Name the blood parasite species.
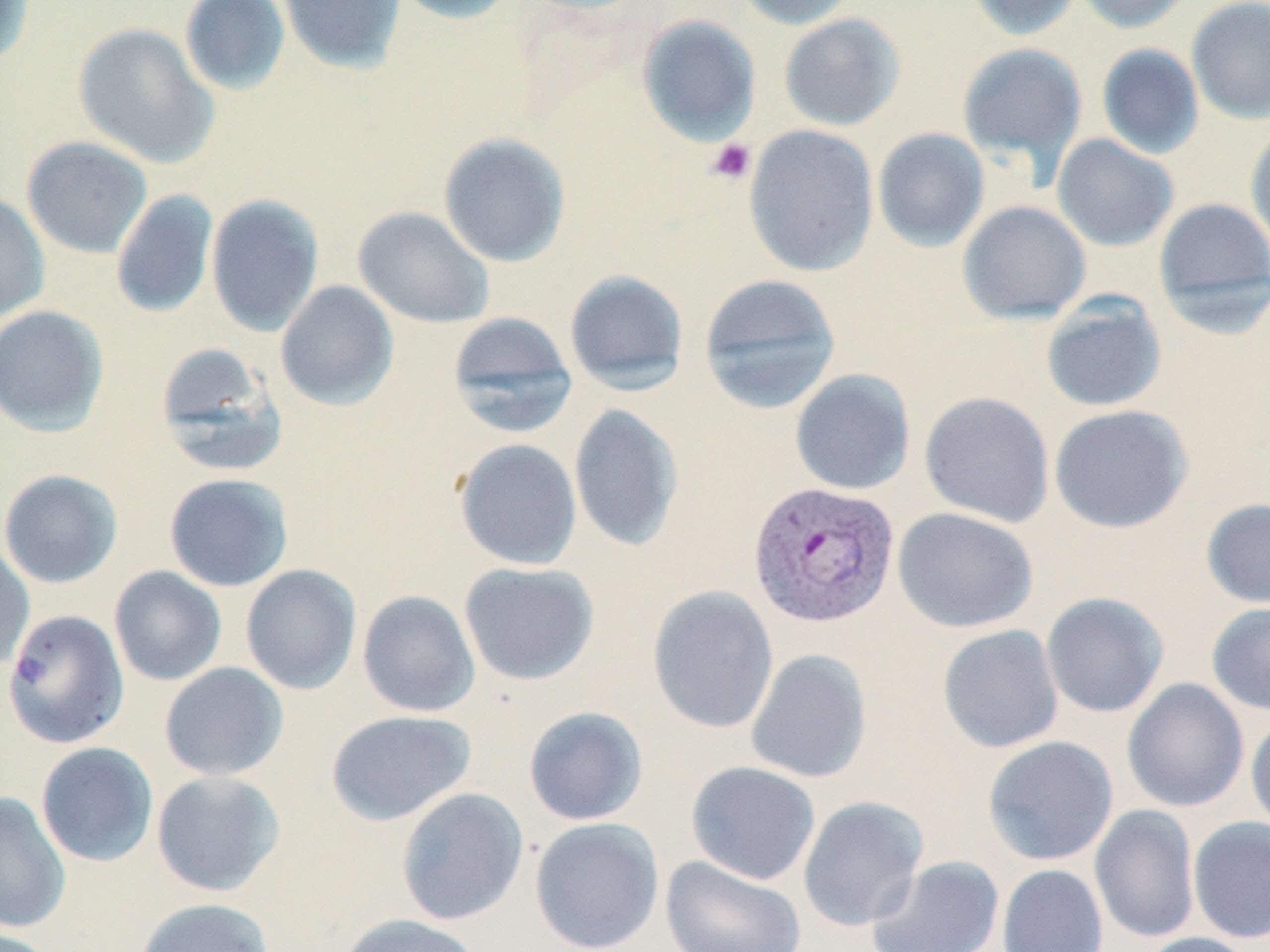

Plasmodium vivax.

Approximate bounding boxes as [x1, y1, x2, y2] in pixels. Plasmodium vivax-infected red blood cell locations: [748, 480, 900, 629]. Uninfected red blood cell locations: [0, 0, 35, 70], [180, 0, 290, 96], [277, 0, 406, 73], [389, 0, 520, 24], [734, 0, 859, 29], [965, 0, 1083, 41], [1075, 0, 1196, 33], [1186, 0, 1270, 123], [779, 13, 906, 131], [637, 15, 761, 145], [73, 22, 219, 168], [957, 42, 1087, 171], [1096, 44, 1204, 159], [743, 124, 879, 277], [1245, 126, 1270, 253], [872, 128, 989, 252], [438, 132, 570, 266], [1051, 134, 1179, 251], [21, 136, 153, 258], [110, 189, 219, 318], [0, 191, 50, 322], [206, 194, 324, 336], [1153, 197, 1270, 319], [957, 200, 1091, 324], [353, 206, 494, 328], [564, 270, 689, 393], [698, 274, 842, 413], [275, 280, 399, 410], [1040, 294, 1167, 412], [0, 305, 109, 437], [447, 311, 578, 438], [155, 342, 289, 477], [789, 368, 916, 495], [919, 392, 1055, 527], [568, 404, 685, 552], [1048, 404, 1193, 533], [454, 438, 582, 570], [0, 469, 123, 588], [163, 473, 293, 592], [1201, 498, 1270, 609], [892, 507, 1038, 633], [0, 538, 34, 672], [459, 561, 599, 686], [240, 564, 362, 695], [109, 566, 227, 686], [647, 585, 779, 734], [357, 590, 480, 717], [1040, 592, 1169, 718], [1207, 602, 1270, 715], [3, 609, 130, 749], [937, 623, 1064, 753], [745, 648, 872, 784], [159, 662, 288, 780], [1122, 677, 1250, 813], [523, 706, 648, 826], [326, 709, 477, 825], [1246, 711, 1270, 839], [982, 735, 1118, 866], [35, 742, 159, 867], [685, 760, 821, 885], [151, 770, 286, 896], [396, 788, 529, 925], [0, 792, 70, 933], [797, 795, 928, 931], [1090, 804, 1200, 944], [1187, 816, 1270, 943], [529, 817, 665, 952], [660, 855, 808, 952], [865, 855, 1005, 952], [997, 863, 1109, 952], [134, 897, 275, 952], [338, 913, 483, 952], [1138, 932, 1259, 952]. Platelet locations: [706, 138, 756, 185]. May-Grünwald-Giemsa-stained preparation. Thin blood smear. 1000x magnification. Single field of view. Image is 1270×952 pixels. Optical microscopy.